Mark where platelets are.
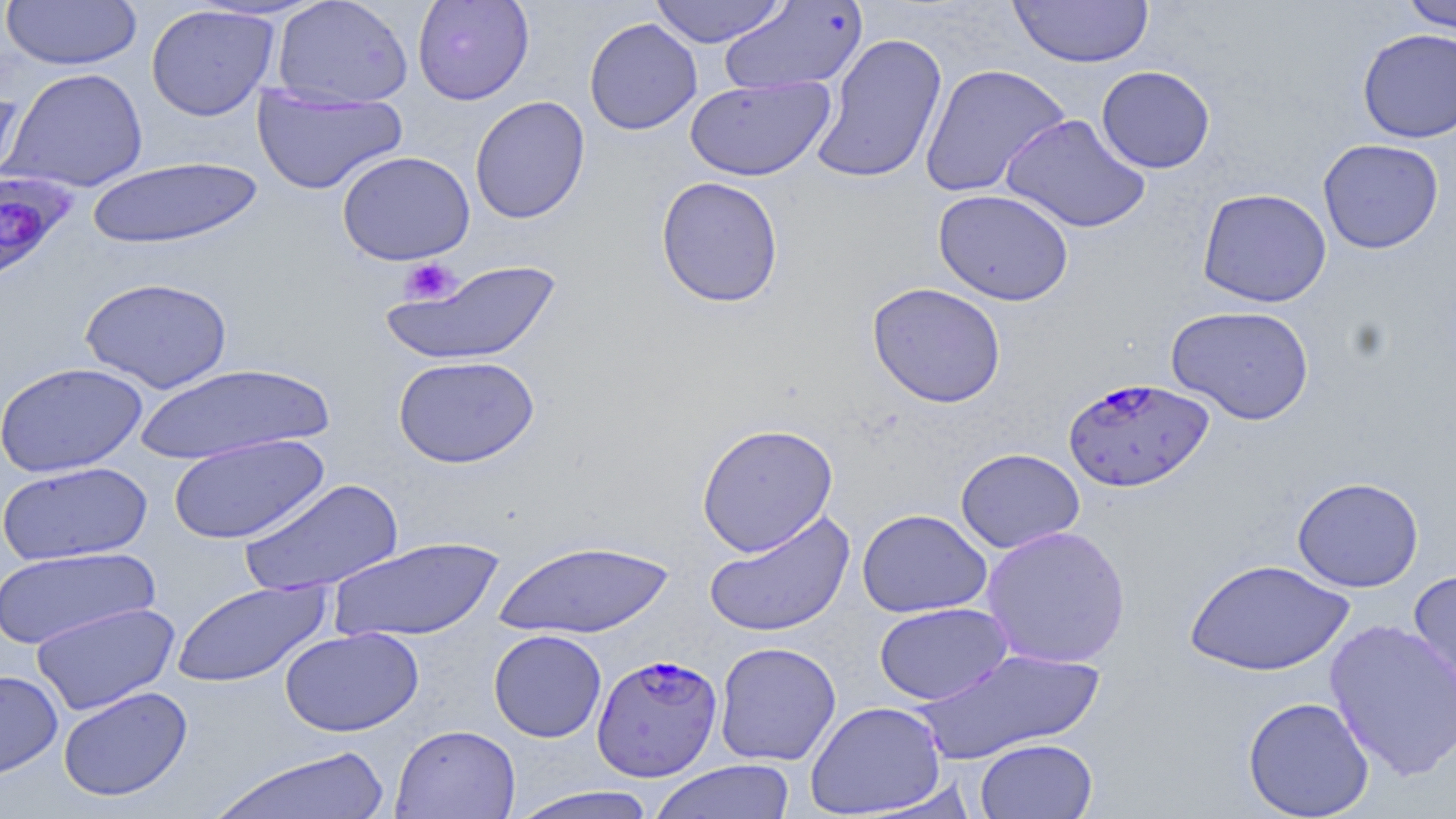
Approximate bounding boxes as (x1,y1)-(x2,y2) corner pairs in pixels.
Platelets: (399,257)-(460,305).

Summary:
  - Plasmodium falciparum-infected red blood cell locations: (0,171)-(78,289), (1062,377)-(1213,492), (591,654)-(723,781)
  - Uninfected red blood cell locations: (1,0)-(142,70), (272,0)-(414,108), (412,0)-(534,105), (649,0)-(788,48), (1008,0)-(1154,68), (1399,0)-(1456,34), (718,2)-(868,96), (146,4)-(280,121), (584,17)-(703,135), (1357,28)-(1456,143), (811,32)-(948,186), (919,64)-(1070,198), (1096,65)-(1215,173), (4,67)-(149,193), (685,76)-(835,181), (0,82)-(25,201), (252,84)-(409,196), (469,95)-(590,224), (1000,113)-(1150,234), (1318,138)-(1443,254), (337,150)-(475,265), (86,156)-(264,250), (655,175)-(784,308), (1197,188)-(1331,307), (933,189)-(1074,306), (380,258)-(562,367), (79,276)-(234,393), (867,282)-(1007,408), (1166,305)-(1314,425), (393,355)-(540,468), (1,361)-(148,478), (133,362)-(335,466), (696,422)-(839,556), (168,433)-(329,545), (955,448)-(1085,553), (1,461)-(153,566), (1292,476)-(1424,592), (238,477)-(405,596), (703,509)-(856,638), (857,509)-(992,618), (981,524)-(1131,669), (327,536)-(506,643), (492,539)-(675,639), (0,546)-(159,651), (1185,557)-(1354,677), (1408,567)-(1456,712), (172,579)-(331,688), (31,601)-(180,715), (874,602)-(1012,705), (1324,617)-(1456,780), (279,626)-(424,737), (488,629)-(607,742), (714,641)-(841,766), (914,648)-(1106,765), (0,669)-(63,780), (57,686)-(193,802), (1242,695)-(1375,818), (805,701)-(948,817), (391,724)-(521,819), (974,738)-(1098,819), (210,745)-(392,819), (647,759)-(798,819), (507,785)-(661,819)
  - Slide-level diagnosis: Plasmodium falciparum
  - Modality: light microscopy
  - Magnification: 1000x
  - Image size: 1456×819 pixels
  - Field of view: single
  - Stain: May-Grünwald-Giemsa
  - Preparation: thin blood smear